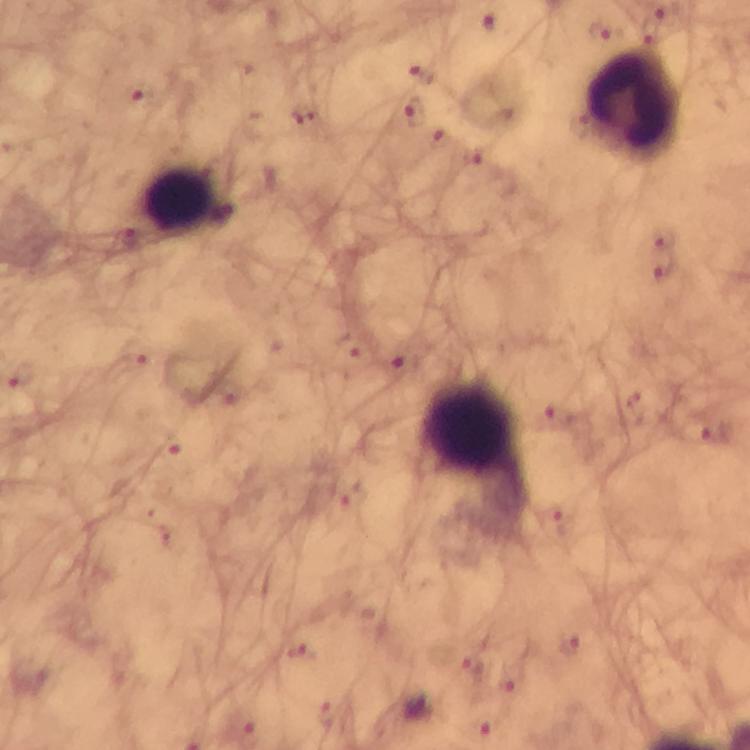
preparation = thick blood smear
capture = smartphone mounted on the microscope
Plasmodium parasite locations = approximate centers as (x, y) in pixels: (490, 21), (420, 76), (414, 112), (665, 267), (405, 361), (558, 416), (718, 436), (569, 644)
context = from a malaria diagnostic workup
magnification = 100x
immersion oil = used
cropped from = a single field of view
stain = Giemsa
image size = 750×750 pixels
leukocyte locations = approximate centers as (x, y) in pixels: (635, 103), (180, 201), (469, 428)